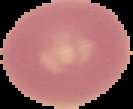 Image is 133×109 pixels. From a thin blood smear. Result: negative for malaria parasites. Segmented cell region on a black background.